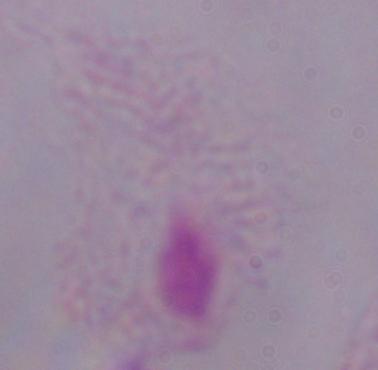 Micrograph. Captured at 1000x magnification. A trichomonad is seen.